Outline each blood parasite and name the species.
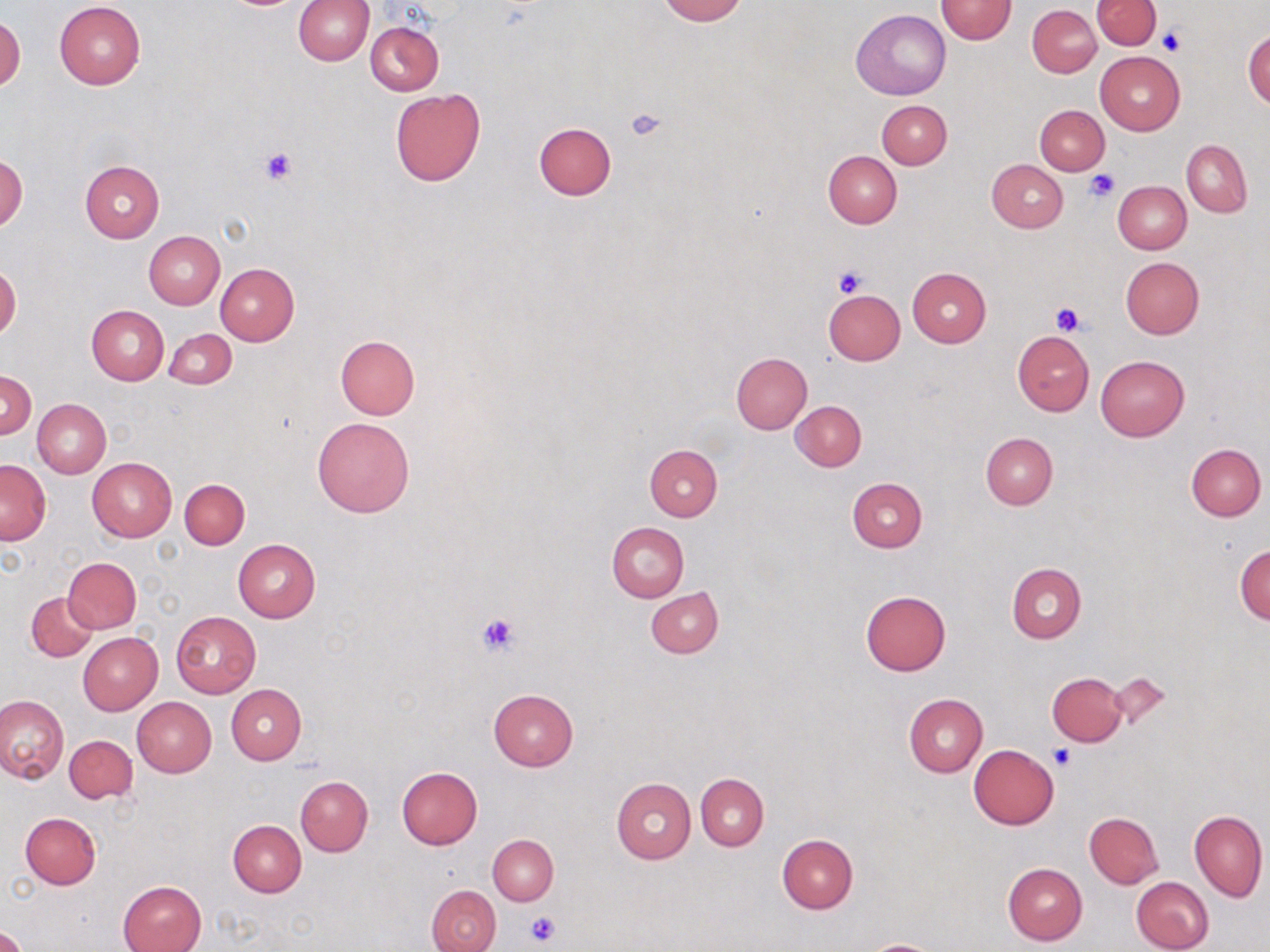
No blood parasites seen.

slide-level diagnosis = no evidence of blood parasites
field of view = single
image size = 1270×952 pixels
magnification = 1000x
uninfected red blood cell locations = approximate bounding boxes as [x1, y1, x2, y2] in pixels: [294, 0, 374, 65], [657, 0, 745, 24], [935, 0, 1016, 44], [1093, 0, 1161, 50], [55, 1, 145, 88], [1028, 5, 1101, 78], [851, 9, 950, 99], [0, 13, 24, 94], [365, 21, 444, 96], [1243, 29, 1270, 109], [1095, 51, 1184, 134], [390, 89, 486, 186], [877, 100, 952, 169], [1035, 105, 1109, 174], [534, 122, 615, 200], [1181, 140, 1252, 217], [823, 150, 901, 228], [0, 155, 26, 233], [987, 159, 1068, 232], [80, 160, 165, 243], [1113, 181, 1191, 254], [144, 231, 225, 310], [1120, 257, 1204, 339], [0, 263, 21, 340], [215, 264, 298, 346], [908, 268, 991, 346], [822, 289, 905, 366], [87, 305, 169, 385], [164, 329, 237, 389], [1012, 330, 1094, 415], [335, 335, 419, 419], [731, 352, 812, 434], [1095, 355, 1188, 440], [1, 371, 36, 438], [33, 398, 111, 478], [791, 400, 867, 471], [312, 417, 415, 518], [981, 432, 1058, 508], [1186, 443, 1266, 521], [645, 444, 722, 521], [87, 458, 177, 541], [0, 459, 51, 545], [847, 477, 927, 552], [180, 478, 250, 549], [606, 523, 688, 602], [233, 538, 321, 622], [1234, 544, 1269, 624], [61, 556, 142, 634], [1006, 563, 1086, 643], [646, 589, 723, 658], [861, 590, 952, 676], [26, 592, 98, 662], [171, 611, 261, 698], [78, 632, 163, 715], [1047, 673, 1128, 746], [1107, 673, 1173, 729], [226, 684, 305, 765], [488, 688, 579, 770], [903, 693, 988, 776], [0, 694, 68, 784], [133, 697, 216, 777], [64, 735, 137, 803], [968, 744, 1059, 830], [397, 765, 483, 849], [696, 774, 768, 850], [296, 776, 372, 855], [613, 778, 697, 863], [1189, 810, 1267, 901], [1084, 812, 1164, 889], [20, 813, 101, 889], [228, 820, 306, 896], [488, 835, 558, 905], [777, 835, 858, 914], [1003, 861, 1086, 945], [1131, 876, 1213, 952], [119, 880, 207, 952], [427, 885, 501, 952], [0, 925, 25, 952], [860, 939, 944, 952]
preparation = thin blood film
stain = May-Grünwald-Giemsa
platelet locations = approximate bounding boxes as [x1, y1, x2, y2] in pixels: [1157, 28, 1185, 57], [626, 106, 667, 142], [260, 147, 298, 184], [1086, 171, 1117, 202], [833, 265, 867, 297], [1050, 301, 1086, 336], [478, 611, 519, 653], [1049, 746, 1075, 770], [524, 912, 559, 946]
modality = light microscopy